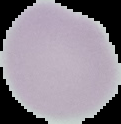

image size = 121×124 pixels
result = no Plasmodium parasites detected
image type = segmented cell region with the area outside set to black
preparation = thin blood smear